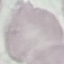 Result: negative for malaria parasites. Automatically extracted cell patch, resized to 64 × 64 pixels. Photographed with a smartphone camera at the microscope eyepiece. Thin blood smear. Giemsa-stained preparation.